Assess this cell for malaria.
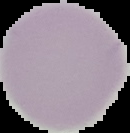

Uninfected.

From a thin blood film. Segmented cell region on a black background. Image is 130×133 pixels.